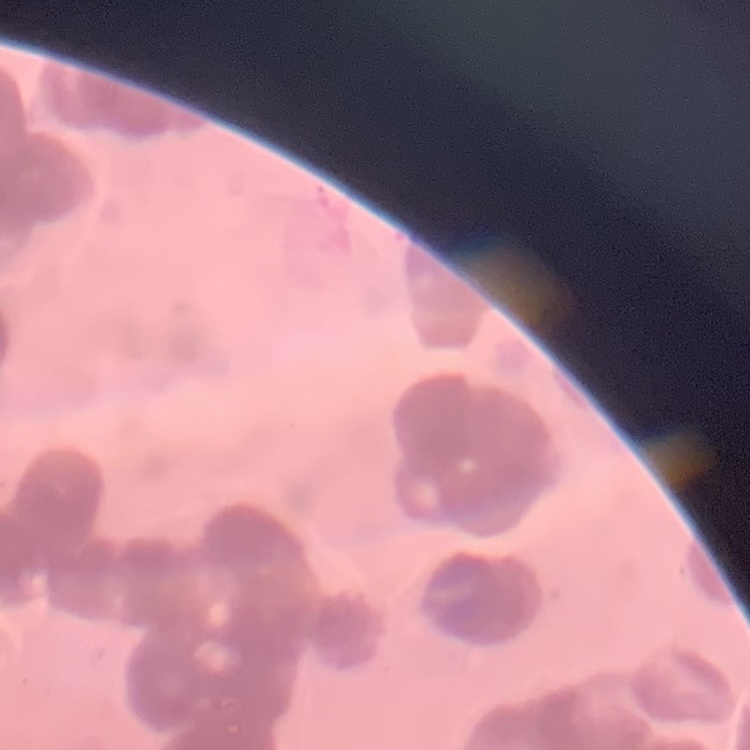 The erythrocytes show rouleaux formation. Field's or Giemsa stain. Thin blood film. One tile cut from a larger photomicrograph.